Locate every blood parasite and identify its species.
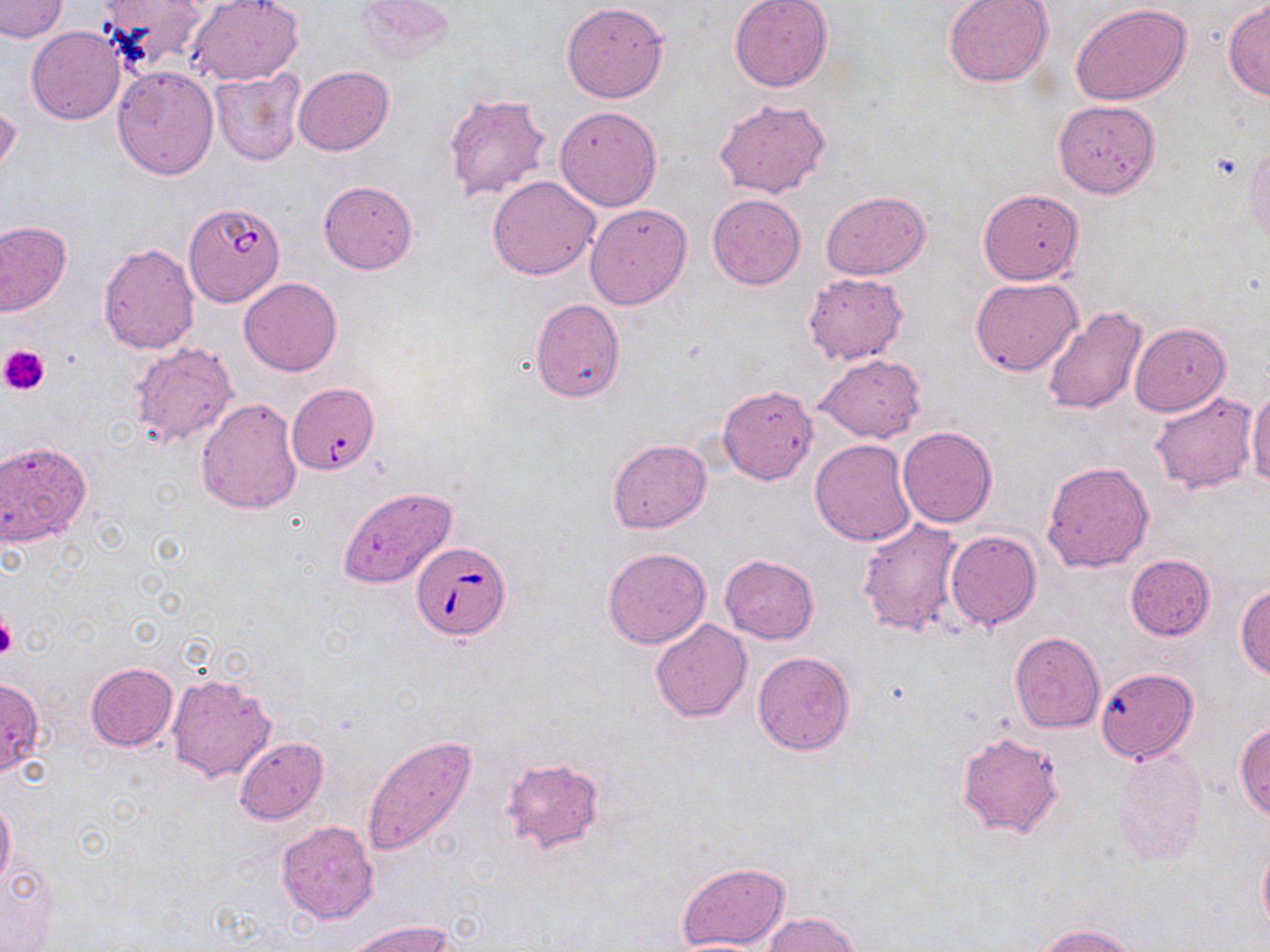
Approximate bounding boxes as (x1, y1, x2, y2) in pixels.
Babesia divergens-infected red blood cells: (184, 202, 284, 306), (412, 542, 509, 640).
No Plasmodium falciparum, Plasmodium ovale, Plasmodium malariae, Plasmodium vivax, or Trypanosoma brucei observed.

Uninfected red blood cell locations: (1, 0, 68, 41), (96, 0, 208, 73), (188, 0, 304, 85), (357, 0, 454, 63), (729, 0, 832, 91), (944, 0, 1054, 87), (561, 2, 668, 103), (1223, 3, 1270, 101), (1071, 5, 1192, 104), (26, 27, 125, 124), (293, 65, 393, 155), (112, 66, 219, 178), (210, 69, 305, 165), (441, 92, 553, 203), (715, 97, 831, 199), (0, 98, 20, 185), (1053, 98, 1160, 198), (555, 105, 661, 210), (1245, 140, 1270, 248), (488, 175, 601, 280), (318, 180, 417, 274), (979, 188, 1084, 284), (820, 190, 930, 279), (708, 194, 806, 289), (585, 203, 692, 309), (0, 220, 71, 317), (98, 242, 200, 353), (802, 273, 908, 366), (970, 277, 1081, 376), (239, 278, 342, 376), (530, 297, 625, 403), (1040, 303, 1150, 415), (1130, 323, 1230, 416), (130, 340, 239, 446), (813, 355, 924, 443), (719, 385, 817, 484), (292, 386, 381, 476), (1247, 388, 1270, 489), (1148, 391, 1257, 494), (197, 399, 302, 512), (897, 426, 997, 529), (0, 439, 91, 548), (608, 439, 712, 534), (810, 439, 916, 546), (1043, 460, 1155, 573), (340, 487, 458, 588), (858, 517, 967, 639), (944, 528, 1041, 630), (603, 548, 711, 649), (720, 554, 818, 643), (1125, 554, 1215, 640), (1236, 583, 1270, 679), (650, 619, 752, 722), (1009, 631, 1104, 732), (753, 651, 854, 755), (86, 663, 177, 751), (1095, 668, 1198, 762), (167, 671, 276, 784), (0, 679, 45, 777), (1235, 721, 1270, 819), (958, 732, 1063, 838), (364, 736, 477, 857), (236, 737, 328, 824), (1113, 748, 1209, 864), (502, 758, 604, 853), (0, 797, 14, 890), (276, 821, 378, 922), (1259, 839, 1270, 935), (1, 861, 58, 949), (679, 862, 789, 949), (765, 912, 861, 951), (349, 918, 452, 952), (1037, 924, 1139, 952), (666, 938, 776, 951). Platelet locations: (0, 344, 51, 397), (0, 612, 17, 661). Slide-level diagnosis: Babesia divergens. Captured at 1000x magnification. Optical microscopy. One field of a larger specimen. May-Grünwald-Giemsa-stained preparation. Image is 1270×952 pixels. Thin blood smear.